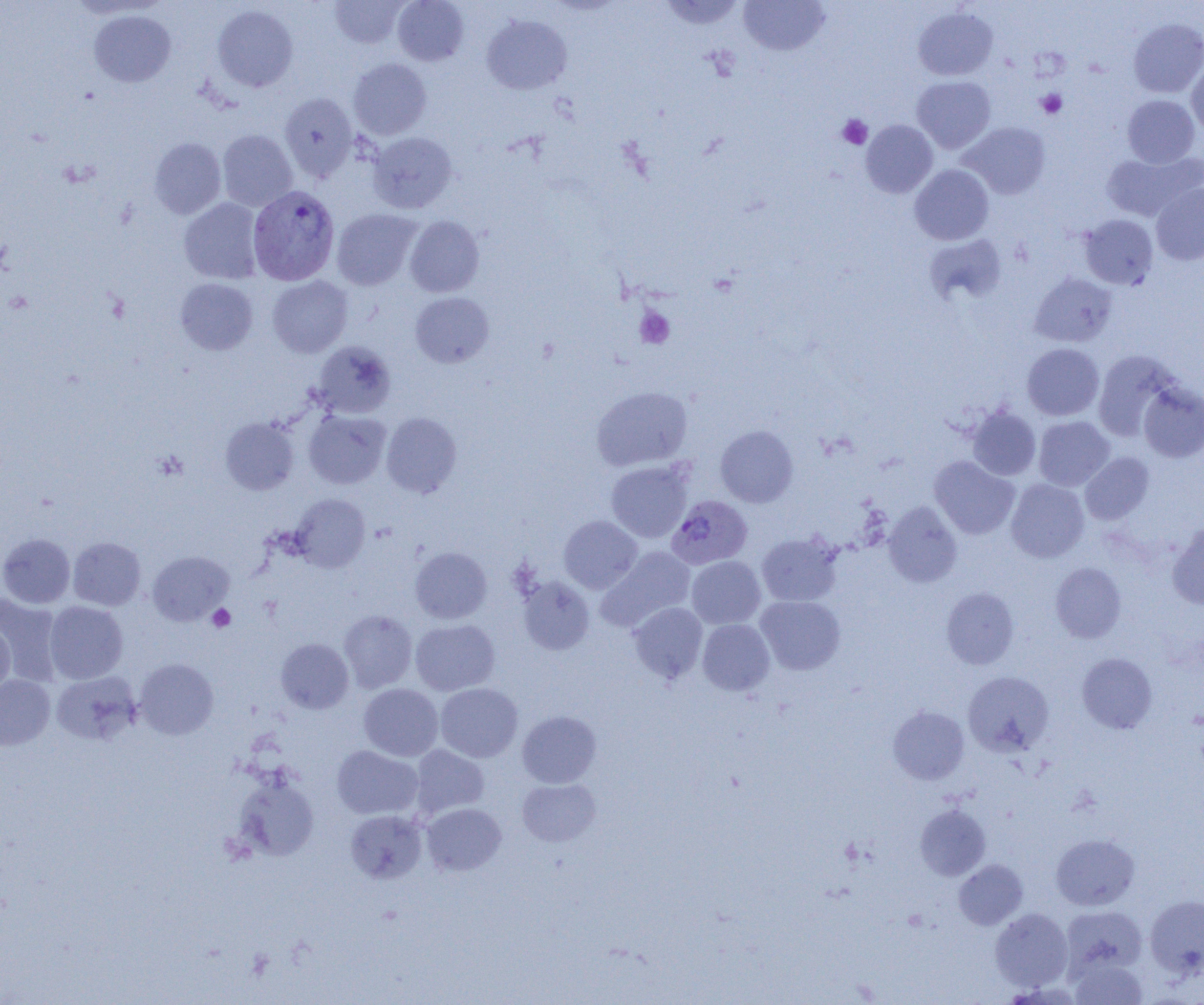

{
  "slide_level_diagnosis": "Plasmodium vivax",
  "magnification": "1000x",
  "image_size": "1204×1005 pixels",
  "modality": "optical microscopy",
  "field_of_view": "single",
  "plasmodium_vivax_infected_red_blood_cell_locations": "approximate bounding boxes as (x1, y1, x2, y2) in pixels: (248, 186, 339, 285), (667, 495, 752, 569)",
  "preparation": "thin blood film",
  "uninfected_red_blood_cell_locations": "approximate bounding boxes as (x1, y1, x2, y2) in pixels: (329, 0, 409, 49), (392, 0, 469, 66), (660, 0, 745, 30), (739, 0, 829, 56), (212, 5, 298, 92), (913, 6, 998, 81), (89, 10, 176, 87), (481, 15, 572, 95), (1129, 18, 1204, 98), (348, 58, 431, 139), (1186, 60, 1204, 138), (912, 76, 995, 153), (280, 93, 358, 181), (1122, 95, 1199, 168), (861, 120, 937, 197), (960, 122, 1050, 199), (217, 129, 298, 211), (367, 132, 457, 213), (149, 138, 226, 219), (1102, 151, 1202, 221), (910, 164, 994, 245), (1151, 183, 1204, 265), (180, 198, 263, 284), (332, 209, 421, 290), (1079, 214, 1158, 289), (405, 215, 484, 296), (925, 234, 1007, 304), (1030, 273, 1117, 347), (267, 275, 352, 357), (175, 278, 257, 355), (410, 292, 494, 368), (311, 341, 395, 418), (1022, 343, 1104, 420), (1093, 350, 1180, 440), (1138, 382, 1204, 462), (591, 386, 692, 471), (968, 406, 1041, 480), (304, 410, 390, 489), (381, 412, 461, 497), (1034, 416, 1115, 490), (220, 417, 299, 495), (715, 425, 799, 507), (1080, 452, 1153, 524), (930, 456, 1019, 539), (606, 460, 693, 543), (1006, 479, 1089, 562), (291, 494, 370, 571), (883, 501, 962, 587), (559, 515, 642, 593), (1167, 522, 1204, 609), (756, 532, 842, 607), (0, 533, 75, 608), (68, 537, 145, 610), (410, 546, 492, 624), (598, 547, 696, 630), (148, 551, 233, 625), (687, 556, 765, 629), (1050, 562, 1126, 643), (518, 576, 594, 655), (941, 587, 1019, 669), (0, 593, 63, 685), (755, 595, 845, 674), (44, 601, 128, 683), (628, 602, 708, 683), (339, 610, 418, 693), (410, 619, 499, 695), (697, 619, 775, 695), (0, 623, 15, 697), (276, 638, 353, 713), (1077, 652, 1157, 733), (134, 658, 219, 739), (51, 670, 141, 745), (963, 671, 1054, 756), (0, 674, 55, 751), (359, 683, 443, 761), (435, 683, 523, 762), (888, 706, 969, 784), (517, 710, 602, 788), (332, 745, 423, 819), (410, 745, 489, 818), (233, 774, 320, 861), (517, 778, 600, 846), (421, 802, 506, 875), (915, 804, 991, 880), (345, 809, 427, 883), (1051, 833, 1140, 910), (954, 859, 1028, 930), (1144, 895, 1204, 978), (1061, 906, 1147, 975), (990, 908, 1073, 991), (1069, 957, 1149, 1005)",
  "platelet_locations": "approximate bounding boxes as (x1, y1, x2, y2) in pixels: (1036, 89, 1067, 119), (837, 114, 872, 149), (635, 306, 675, 348), (207, 604, 235, 632)"
}